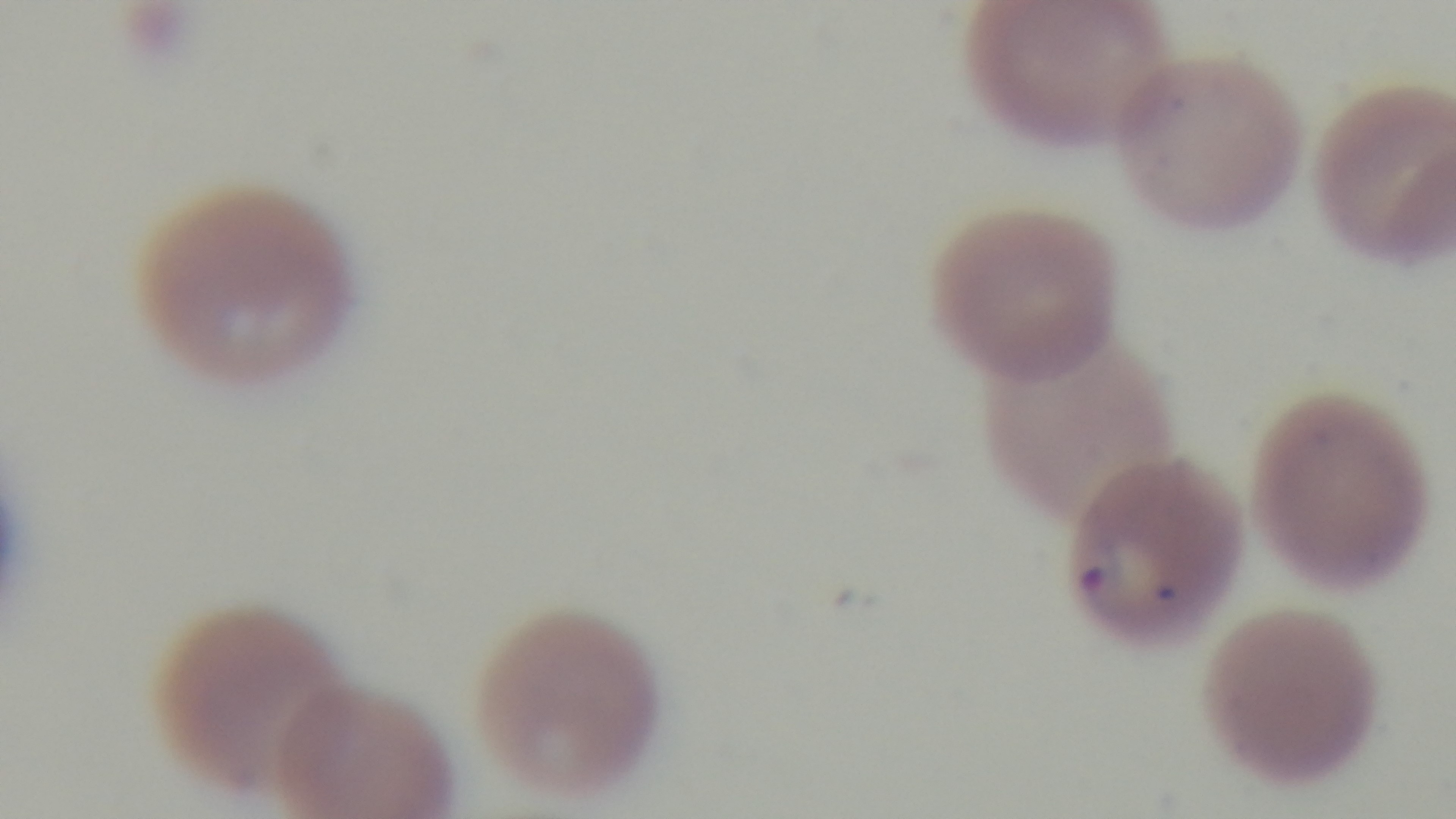
Summary:
  - Capture: mounted 4K digital camera
  - Malaria status: infected
  - Modality: light microscopy
  - Field of view: one from the slide
  - Objective: 100x oil immersion
  - Preparation: thin smear
  - Stain: Giemsa